Locate and identify every blood parasite.
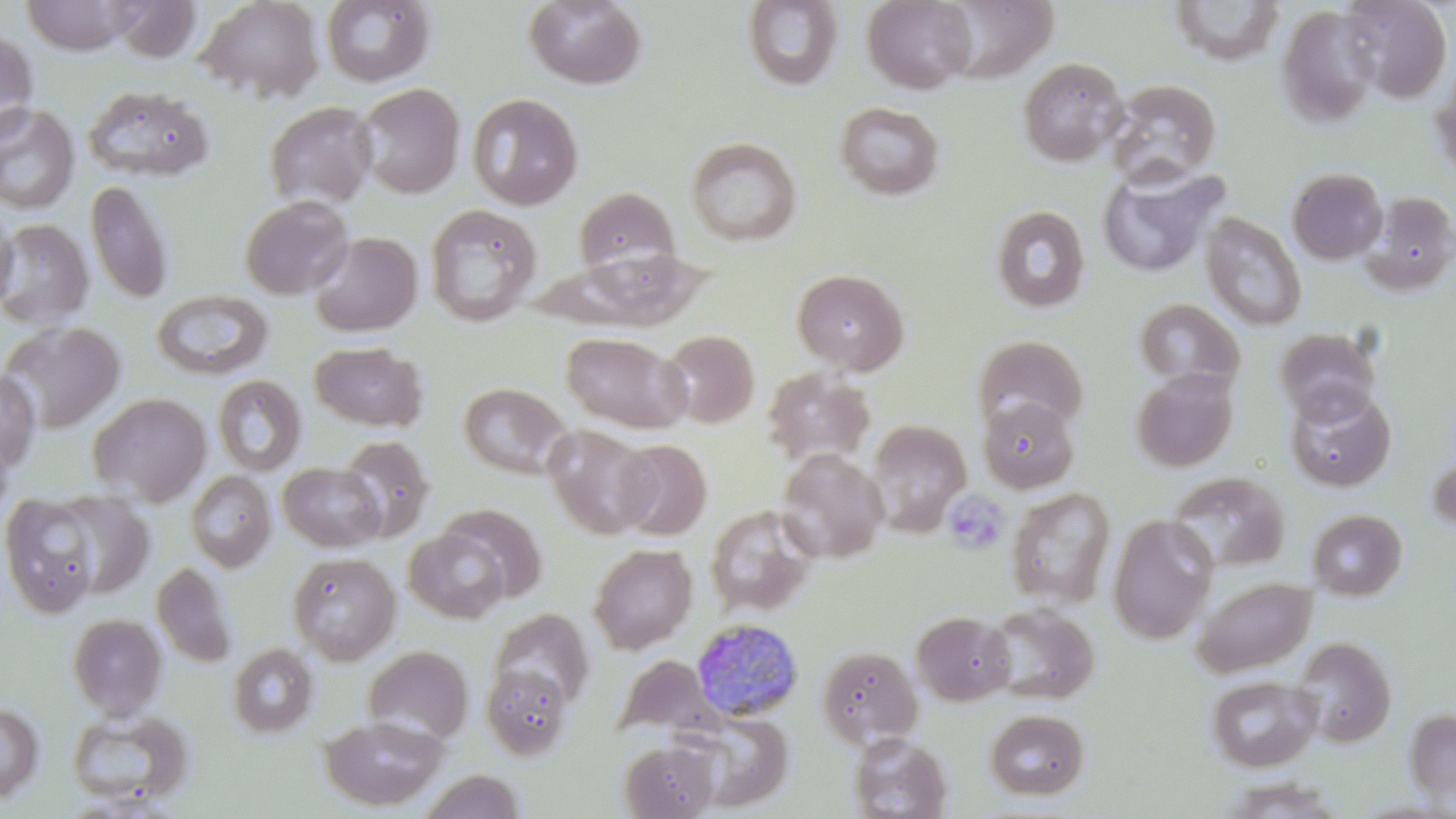

Approximate bounding boxes as named x1/y1/x2/y2 corners in pixels.
Plasmodium malariae-infected red blood cells: (x1=691, y1=618, x2=804, y2=722).
No Plasmodium falciparum, Plasmodium ovale, Plasmodium vivax, Babesia divergens, or Trypanosoma brucei observed.

slide-level diagnosis = Plasmodium malariae
image size = 1456×819 pixels
stain = May-Grünwald-Giemsa
magnification = 1000x
preparation = thin blood film
uninfected red blood cell locations = approximate bounding boxes as named x1/y1/x2/y2 corners in pixels: (x1=21, y1=0, x2=137, y2=55), (x1=195, y1=0, x2=323, y2=103), (x1=524, y1=0, x2=647, y2=90), (x1=862, y1=0, x2=976, y2=93), (x1=111, y1=1, x2=201, y2=62), (x1=320, y1=1, x2=436, y2=87), (x1=741, y1=1, x2=844, y2=92), (x1=1339, y1=1, x2=1452, y2=103), (x1=1275, y1=5, x2=1381, y2=130), (x1=0, y1=29, x2=39, y2=143), (x1=1017, y1=57, x2=1127, y2=166), (x1=1429, y1=65, x2=1456, y2=185), (x1=1105, y1=78, x2=1222, y2=188), (x1=357, y1=82, x2=465, y2=198), (x1=82, y1=85, x2=215, y2=182), (x1=467, y1=93, x2=584, y2=211), (x1=263, y1=100, x2=378, y2=210), (x1=834, y1=102, x2=945, y2=201), (x1=0, y1=103, x2=80, y2=214), (x1=686, y1=137, x2=802, y2=247), (x1=1096, y1=164, x2=1224, y2=279), (x1=1286, y1=167, x2=1388, y2=265), (x1=86, y1=180, x2=173, y2=304), (x1=573, y1=186, x2=680, y2=277), (x1=1359, y1=191, x2=1456, y2=297), (x1=239, y1=195, x2=353, y2=300), (x1=424, y1=204, x2=541, y2=327), (x1=990, y1=204, x2=1091, y2=314), (x1=0, y1=205, x2=18, y2=314), (x1=1201, y1=212, x2=1307, y2=330), (x1=0, y1=219, x2=94, y2=330), (x1=309, y1=231, x2=423, y2=336), (x1=553, y1=247, x2=710, y2=330), (x1=792, y1=268, x2=909, y2=375), (x1=152, y1=289, x2=273, y2=380), (x1=1133, y1=297, x2=1245, y2=393), (x1=0, y1=320, x2=125, y2=433), (x1=1275, y1=327, x2=1381, y2=426), (x1=660, y1=329, x2=760, y2=428), (x1=561, y1=332, x2=691, y2=433), (x1=972, y1=334, x2=1089, y2=434), (x1=310, y1=341, x2=429, y2=431), (x1=1130, y1=367, x2=1239, y2=472), (x1=0, y1=368, x2=41, y2=473), (x1=761, y1=368, x2=875, y2=468), (x1=212, y1=375, x2=307, y2=476), (x1=458, y1=382, x2=573, y2=480), (x1=1284, y1=386, x2=1397, y2=492), (x1=86, y1=392, x2=212, y2=507), (x1=977, y1=396, x2=1079, y2=493), (x1=868, y1=419, x2=971, y2=535), (x1=543, y1=424, x2=659, y2=538), (x1=0, y1=428, x2=15, y2=528), (x1=337, y1=435, x2=434, y2=541), (x1=615, y1=439, x2=712, y2=540), (x1=775, y1=448, x2=888, y2=563), (x1=277, y1=462, x2=386, y2=552), (x1=185, y1=470, x2=276, y2=572), (x1=1166, y1=471, x2=1290, y2=573), (x1=1005, y1=488, x2=1116, y2=609), (x1=47, y1=491, x2=154, y2=602), (x1=1, y1=492, x2=107, y2=617), (x1=431, y1=504, x2=547, y2=605), (x1=704, y1=504, x2=819, y2=617), (x1=1307, y1=509, x2=1407, y2=601), (x1=1107, y1=514, x2=1218, y2=644), (x1=404, y1=526, x2=515, y2=623), (x1=588, y1=543, x2=698, y2=654), (x1=288, y1=552, x2=401, y2=665), (x1=151, y1=561, x2=237, y2=668), (x1=1191, y1=575, x2=1317, y2=677), (x1=985, y1=603, x2=1099, y2=704), (x1=488, y1=608, x2=594, y2=709), (x1=912, y1=610, x2=1016, y2=706), (x1=67, y1=613, x2=168, y2=719), (x1=1293, y1=637, x2=1397, y2=747), (x1=227, y1=643, x2=320, y2=739), (x1=362, y1=644, x2=474, y2=746), (x1=816, y1=645, x2=922, y2=748), (x1=614, y1=655, x2=717, y2=739), (x1=481, y1=665, x2=574, y2=761), (x1=1206, y1=674, x2=1322, y2=772), (x1=0, y1=701, x2=44, y2=804), (x1=65, y1=707, x2=193, y2=810), (x1=984, y1=708, x2=1090, y2=800), (x1=1402, y1=708, x2=1456, y2=808), (x1=680, y1=710, x2=793, y2=811), (x1=318, y1=714, x2=447, y2=811), (x1=848, y1=732, x2=953, y2=818), (x1=618, y1=740, x2=719, y2=818), (x1=419, y1=770, x2=527, y2=819), (x1=1219, y1=777, x2=1345, y2=819)
field of view = single
platelet locations = approximate bounding boxes as named x1/y1/x2/y2 corners in pixels: (x1=942, y1=490, x2=1011, y2=556)
modality = optical microscopy